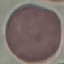

result = no malaria parasites detected
stain = Giemsa
preparation = thin blood film
capture = smartphone through the microscope eyepiece
image type = cell patch, automatically extracted from a larger field of view and resized to 64 × 64 pixels